Locate and identify every blood parasite.
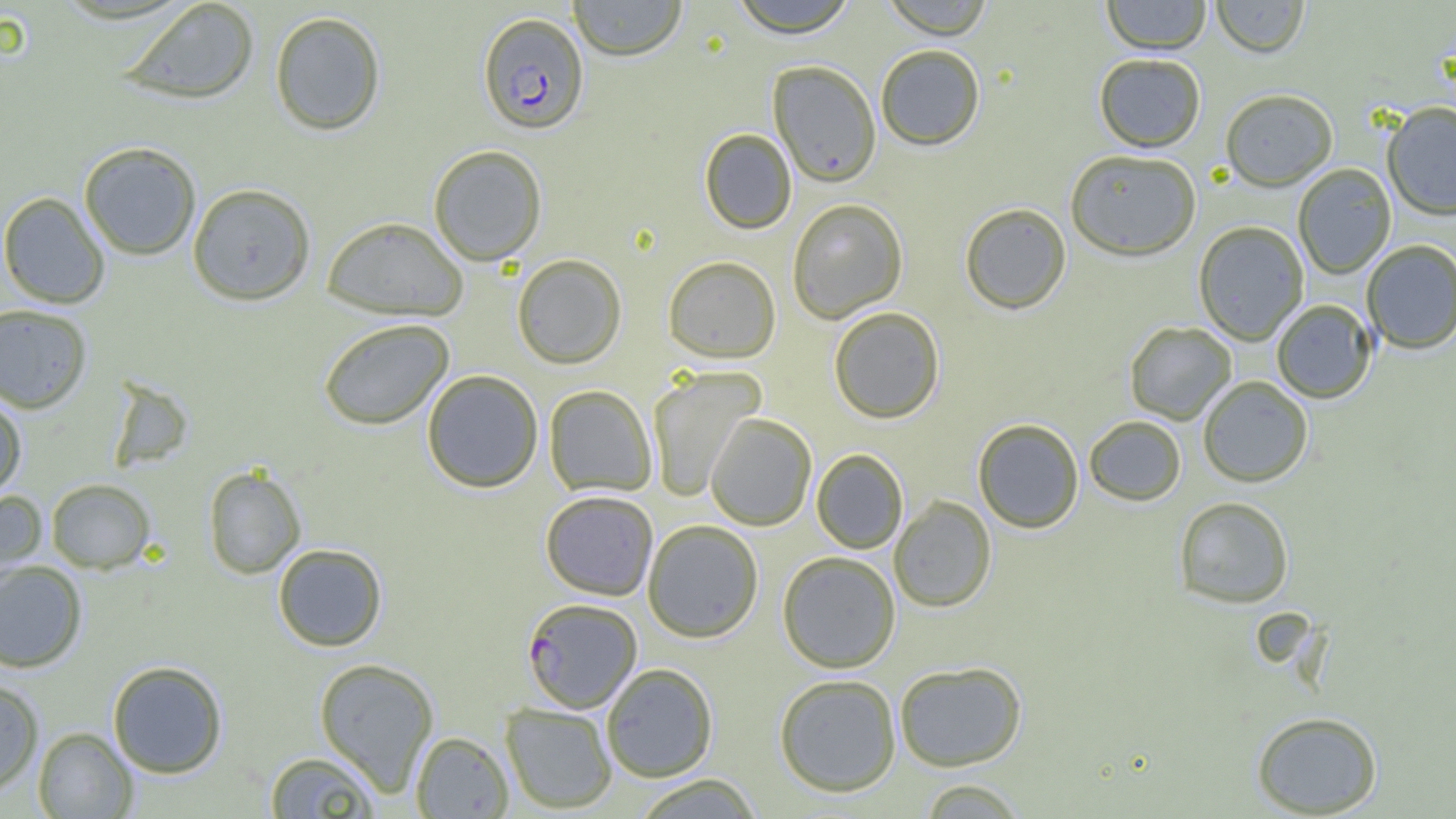
Approximate bounding boxes as [x1, y1, x2, y2] in pixels.
Plasmodium falciparum-infected red blood cells: [477, 12, 589, 135], [521, 597, 642, 714].
No Plasmodium ovale, Plasmodium malariae, Plasmodium vivax, Babesia divergens, or Trypanosoma brucei observed.

slide_level_diagnosis: Plasmodium falciparum
field_of_view: single
magnification: 1000x
image_size: 1456×819 pixels
modality: optical microscopy
preparation: thin blood smear
uninfected_red_blood_cell_locations: 'approximate bounding boxes as [x1, y1, x2, y2] in pixels: [120, 0, 260, 105], [568, 0, 688, 61], [728, 0, 859, 37], [880, 0, 995, 39], [1101, 0, 1211, 55], [1211, 0, 1310, 58], [269, 10, 387, 136], [875, 44, 985, 151], [1094, 54, 1206, 152], [768, 60, 881, 187], [1220, 89, 1338, 192], [1380, 100, 1456, 354], [1382, 102, 1456, 221], [699, 128, 797, 234], [78, 141, 202, 261], [428, 145, 547, 266], [1065, 149, 1201, 261], [1293, 163, 1396, 279], [187, 183, 316, 306], [0, 192, 110, 309], [787, 198, 908, 323], [959, 203, 1072, 315], [322, 216, 468, 321], [1193, 221, 1309, 345], [1361, 239, 1456, 354], [512, 254, 627, 369], [663, 256, 782, 362], [1271, 299, 1377, 403], [0, 303, 93, 413], [828, 307, 945, 424], [318, 318, 454, 430], [1124, 321, 1236, 424], [646, 366, 765, 501], [421, 369, 544, 493], [1198, 376, 1313, 487], [543, 385, 658, 497], [0, 397, 27, 499], [705, 413, 817, 531], [1084, 416, 1186, 506], [973, 419, 1084, 534], [812, 449, 908, 554], [203, 466, 306, 579], [46, 478, 156, 574], [0, 488, 47, 591], [540, 490, 659, 600], [1174, 496, 1294, 608], [889, 497, 996, 612], [642, 519, 763, 643], [272, 543, 388, 652], [777, 551, 901, 673], [0, 561, 88, 672], [314, 657, 440, 795], [107, 660, 228, 778], [894, 661, 1027, 771], [601, 663, 718, 782], [774, 673, 902, 797], [0, 679, 44, 795], [500, 702, 617, 814], [1251, 710, 1383, 817], [33, 727, 138, 818], [410, 731, 514, 818], [264, 750, 382, 818], [630, 774, 764, 818], [917, 778, 1029, 818]'